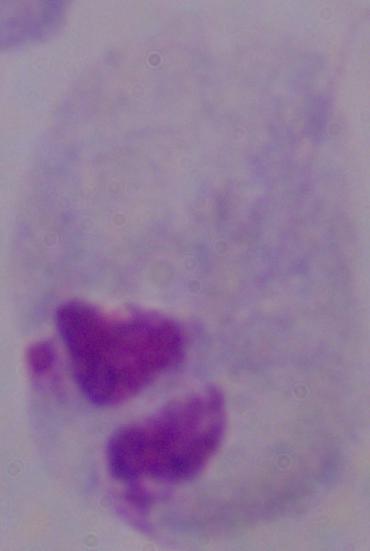
magnification = 1000x
modality = micrograph
identification = trichomonad